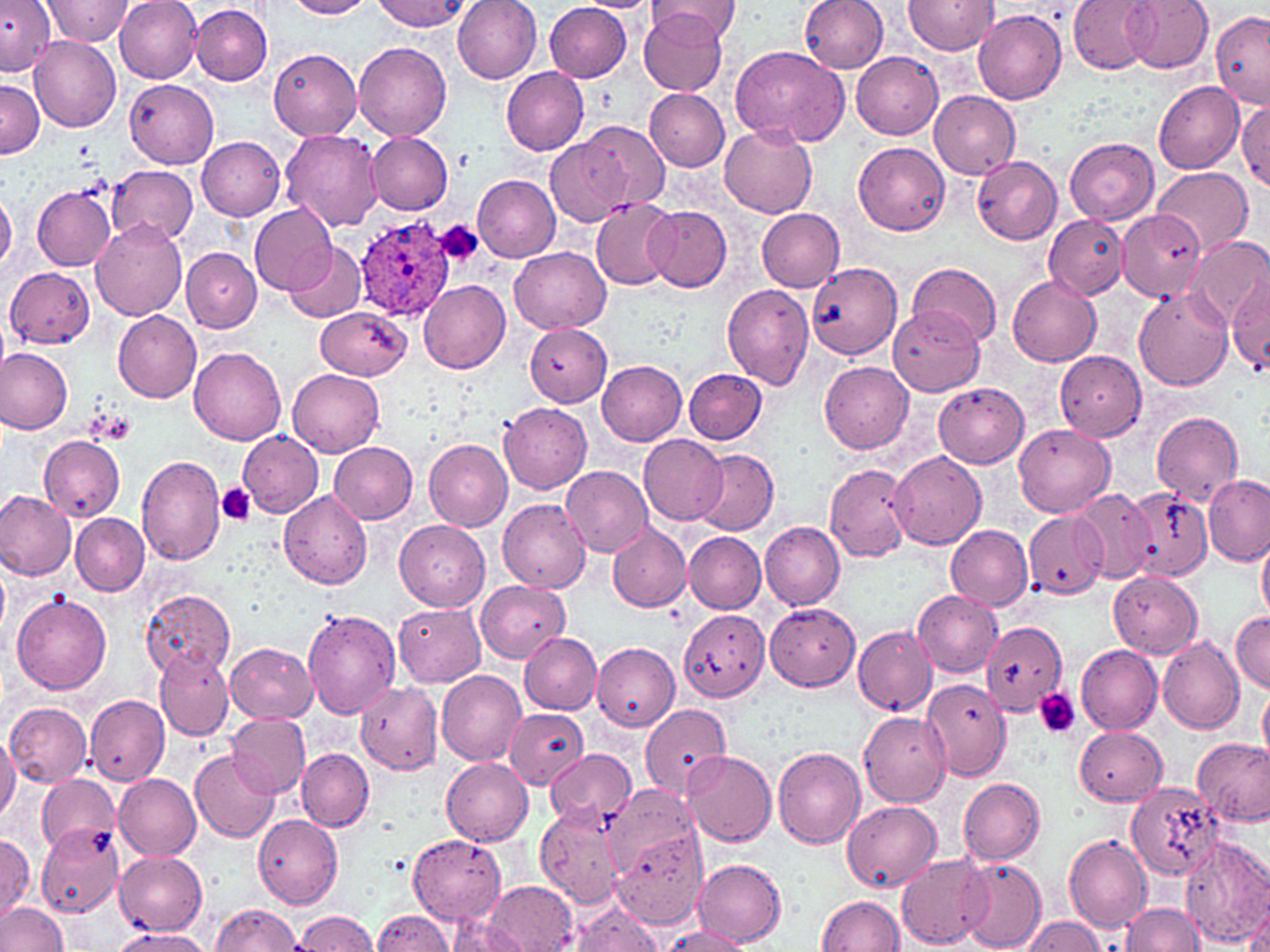
Approximate bounding boxes as (x1,y1)-(x2,y2) corner pairs in pixels. Platelet locations: (433,220)-(484,267), (86,411)-(132,444), (216,482)-(256,525), (1034,687)-(1081,739). Uninfected red blood cell locations: (40,0)-(131,45), (115,0)-(203,83), (287,0)-(374,19), (377,0)-(467,30), (453,0)-(542,86), (577,0)-(659,13), (647,0)-(741,46), (800,0)-(889,73), (904,0)-(998,54), (1068,0)-(1158,74), (1123,0)-(1213,74), (0,2)-(56,76), (191,3)-(272,84), (544,3)-(632,82), (638,8)-(729,96), (975,11)-(1066,105), (1211,11)-(1270,104), (30,34)-(121,132), (354,39)-(452,140), (727,45)-(848,147), (268,49)-(363,140), (851,51)-(943,139), (501,68)-(590,155), (1,78)-(42,159), (124,79)-(219,169), (1153,80)-(1245,173), (645,88)-(730,170), (930,91)-(1021,179), (1235,102)-(1269,192), (576,122)-(669,214), (719,123)-(816,218), (279,128)-(384,234), (368,132)-(453,215), (547,133)-(637,226), (198,137)-(285,221), (1064,138)-(1159,225), (853,141)-(950,233), (973,156)-(1062,245), (108,165)-(198,243), (1153,167)-(1253,256), (473,174)-(562,261), (32,185)-(116,270), (0,193)-(17,270), (590,199)-(679,290), (248,203)-(338,295), (645,206)-(731,291), (756,208)-(846,292), (1118,211)-(1205,301), (1044,215)-(1128,299), (90,220)-(186,323), (1190,236)-(1270,328), (284,243)-(367,323), (510,248)-(611,334), (182,250)-(261,332), (804,261)-(902,361), (908,261)-(1001,348), (7,267)-(96,349), (1007,276)-(1101,368), (1230,279)-(1270,375), (419,280)-(511,373), (722,285)-(815,389), (1133,288)-(1233,391), (316,305)-(410,379), (890,308)-(983,395), (114,311)-(203,402), (525,324)-(611,406), (1,347)-(73,434), (189,347)-(286,445), (1055,351)-(1146,441), (597,360)-(687,446), (819,361)-(913,454), (684,368)-(767,444), (288,369)-(385,457), (933,381)-(1029,468), (500,403)-(592,494), (1152,412)-(1245,503), (1015,423)-(1116,518), (237,430)-(323,517), (639,434)-(729,525), (40,435)-(125,522), (425,439)-(513,530), (329,441)-(418,523), (692,448)-(779,534), (889,452)-(987,551), (135,455)-(226,568), (824,462)-(914,562), (562,465)-(653,557), (1202,474)-(1269,565), (0,488)-(76,580), (1070,488)-(1155,583), (1123,488)-(1213,582), (279,491)-(372,591), (498,498)-(590,593), (1024,510)-(1109,596), (72,514)-(149,595), (394,519)-(490,610), (761,522)-(845,609), (607,523)-(690,611), (946,523)-(1033,611), (684,532)-(766,613), (1257,539)-(1270,621), (1,561)-(9,637), (1108,570)-(1203,658), (476,580)-(568,662), (141,589)-(237,678), (913,589)-(1004,676), (11,594)-(111,695), (395,603)-(486,686), (766,603)-(860,690), (678,609)-(770,702), (302,610)-(401,719), (1231,611)-(1270,693), (981,622)-(1067,716), (853,625)-(936,716), (519,632)-(601,714), (1157,635)-(1245,736), (227,643)-(317,722), (593,643)-(679,731), (1076,644)-(1164,734), (156,650)-(234,739), (436,670)-(526,768), (922,678)-(1012,782), (356,683)-(442,774), (1259,685)-(1270,763), (87,693)-(169,786), (640,702)-(731,798), (5,703)-(91,787), (504,707)-(586,788), (859,710)-(951,806), (227,712)-(310,799), (1074,726)-(1167,805), (0,732)-(18,823), (1192,738)-(1270,826), (773,747)-(865,849), (546,748)-(636,828), (189,749)-(280,844), (298,749)-(375,831), (683,750)-(776,847), (441,756)-(534,846), (113,773)-(201,859), (37,776)-(119,855), (958,778)-(1046,865), (1129,783)-(1223,882), (607,784)-(702,876), (842,800)-(940,892), (535,802)-(628,908), (253,813)-(343,909), (39,827)-(125,915), (611,828)-(709,927), (0,834)-(35,921), (408,834)-(506,926), (1064,835)-(1152,932), (1180,837)-(1270,947), (116,850)-(208,934), (897,852)-(993,948), (693,857)-(785,946), (957,859)-(1046,951), (486,882)-(577,951), (1245,894)-(1270,951), (817,895)-(903,951), (0,901)-(69,952), (566,901)-(664,952), (1123,901)-(1205,952), (211,904)-(303,952), (297,909)-(379,951), (371,910)-(455,952), (446,915)-(529,952), (1025,916)-(1107,952), (661,926)-(751,952), (111,928)-(215,952). Plasmodium ovale-infected red blood cell locations: (355,215)-(457,322). Slide-level diagnosis: Plasmodium ovale. Image is 1270×952 pixels. Optical microscopy. Single field of view. May-Grünwald-Giemsa-stained preparation. Captured at 1000x magnification. Thin blood smear.